Identify the parasite.
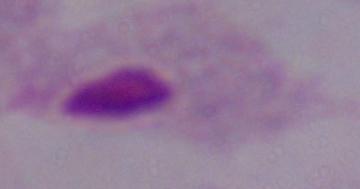

This is a trichomonad.

{
  "magnification": "1000x",
  "modality": "micrograph"
}